Give the position of every malaria parasite.
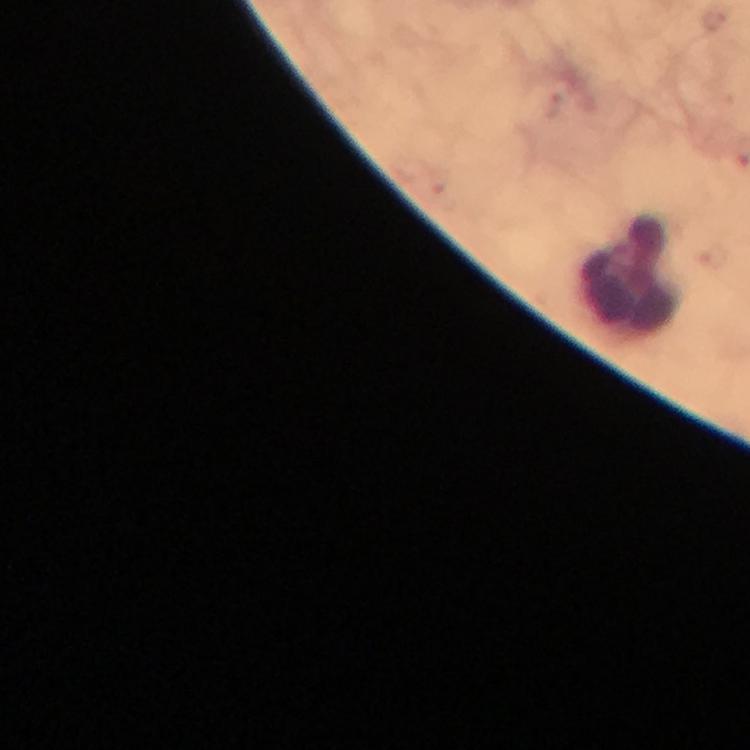
No malaria parasites detected.

image size = 750×750 pixels
context = from a malaria diagnostic workup
magnification = 100x
cropped from = a single field of view
immersion oil = applied
stain = Giemsa
leukocyte locations = approximate centers as (x, y) in pixels: (633, 277)
capture = smartphone mounted on the microscope
preparation = thick smear